Give the position of every leukocyte visible.
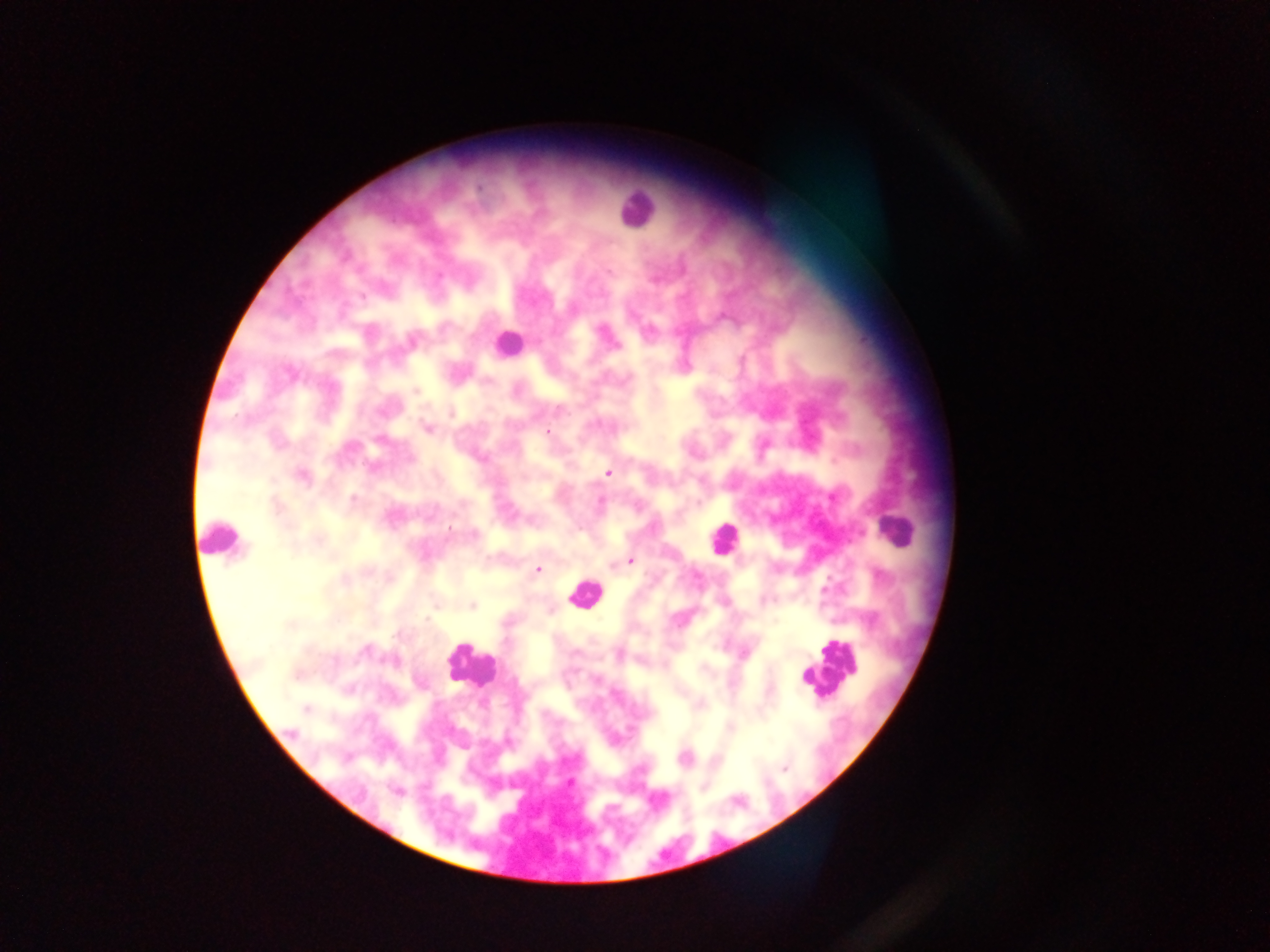

Approximate centers as x y in pixels.
Leukocytes: 636 208; 508 344; 896 532; 220 538; 723 539; 583 593; 470 663; 829 670.

Summary:
  - Plasmodium parasite locations: 411 339; 415 391; 451 413; 427 428; 547 432; 608 473; 300 475; 629 560; 537 569; 471 605; 698 704; 306 708; 730 727; 684 757; 784 767; 569 782; 703 786
  - Preparation: thick blood smear
  - Capture: mobile-phone photograph through a microscope
  - Image size: 1270×952 pixels
  - Field of view: single
  - Country: Ghana